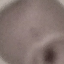
result = negative for malaria parasites
capture = smartphone through the microscope eyepiece
stain = Giemsa
image type = automatically extracted cell patch, resized to 64 × 64 pixels
preparation = thin blood smear